State which cell type is depicted.
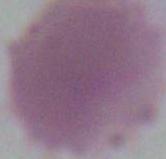
An erythrocyte.

Captured at 1000x magnification. Photomicrograph.